Describe the morphology of the red blood cells.
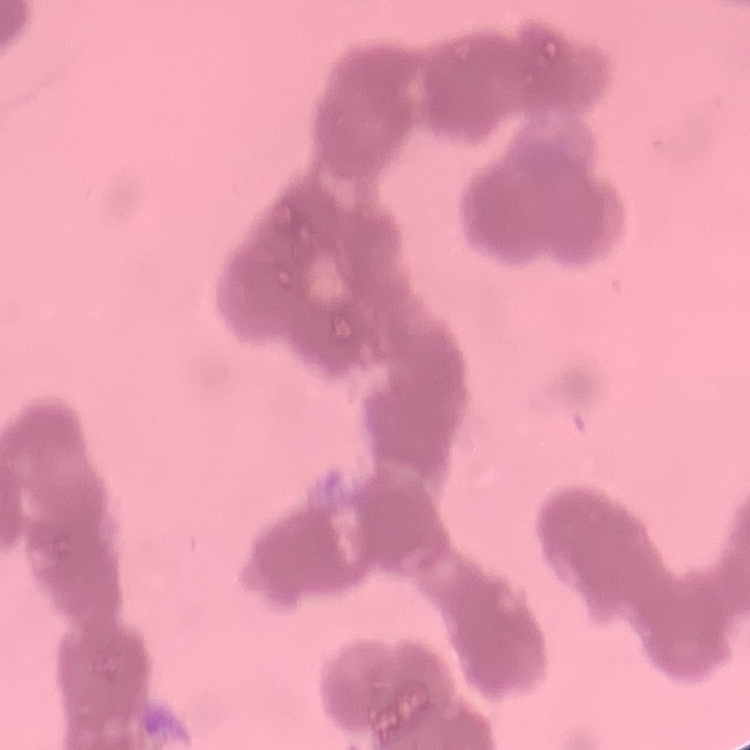
Rouleaux formation.

Summary:
  - Stain: Field's or Giemsa
  - Preparation: thin peripheral smear
  - Image type: one tile cut from a larger photomicrograph